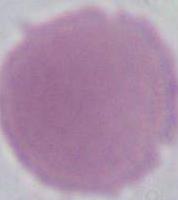

Micrograph. A red blood cell is shown. Captured at 1000x magnification.